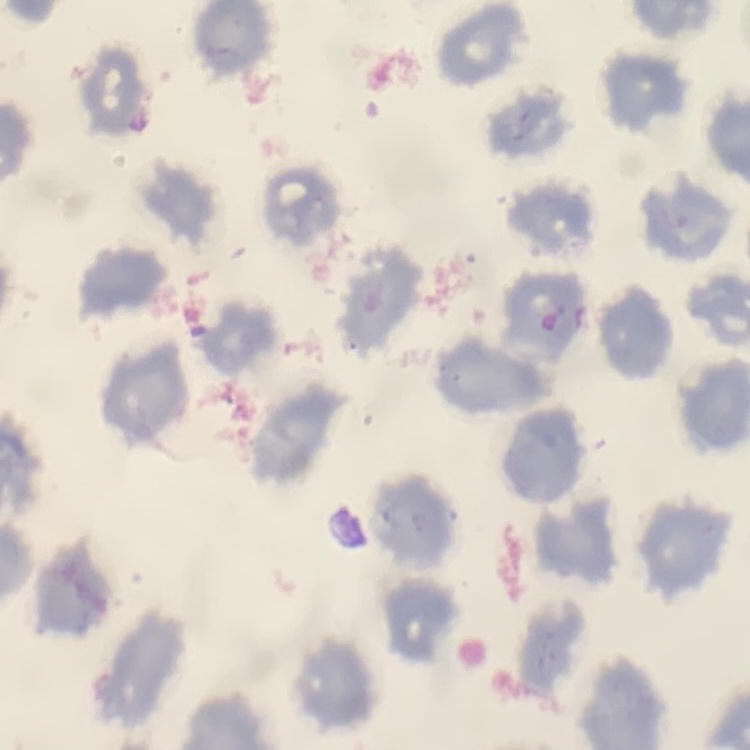
Summary:
  - Erythrocyte morphology: no rouleaux formation
  - Stain: Field's or Giemsa
  - Preparation: thin peripheral smear
  - Image type: square crop of a larger photomicrograph